Comment on the morphology of the erythrocytes.
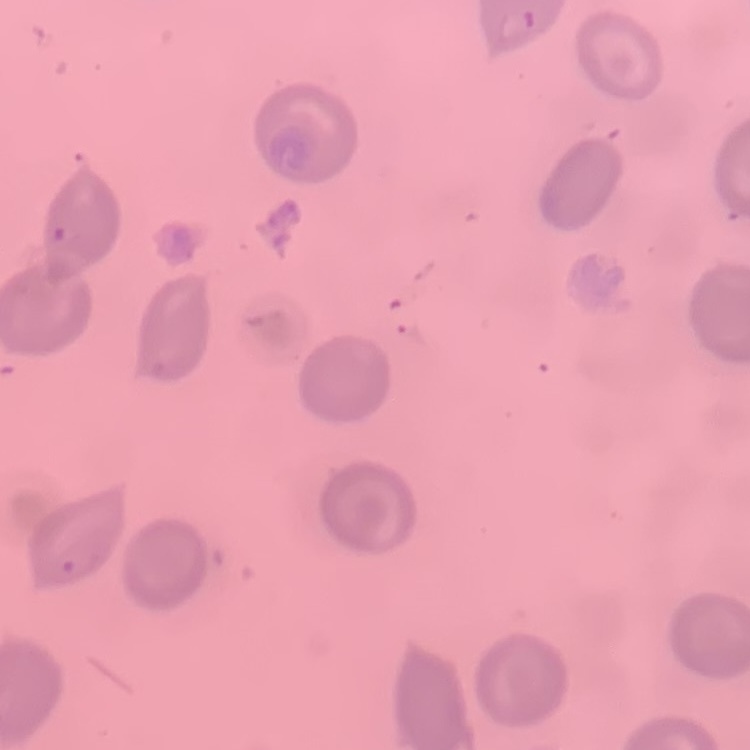

No rouleaux formation.

Summary:
  - Stain: Field's or Giemsa
  - Image type: square crop of a larger photomicrograph
  - Preparation: thin peripheral smear